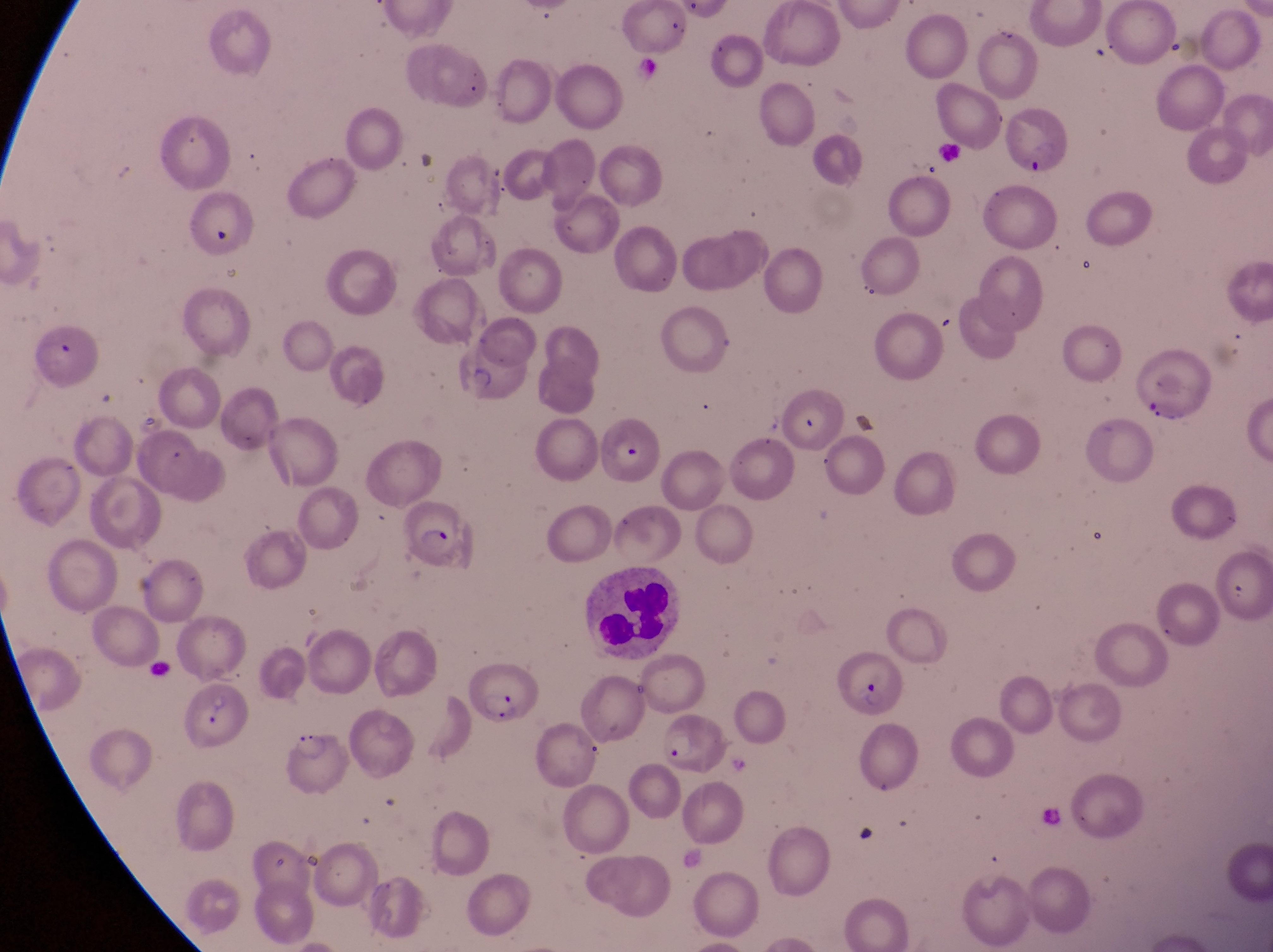

artifact (platelet-like body, stain precipitate, or debris) locations = approximate bounding boxes as [left, top, right, bottom] in pixels: [209, 222, 242, 254]
field of view = single
preparation = thin blood film
capture = smartphone photograph through the eyepiece of an Olympus CX-23 microscope
parasitised red blood cell locations = approximate bounding boxes as [left, top, right, bottom] in pixels: [1000, 109, 1074, 180], [30, 325, 95, 385], [447, 335, 534, 403], [594, 414, 657, 486], [395, 502, 473, 572], [838, 647, 908, 717], [459, 657, 546, 722], [183, 686, 245, 763], [657, 711, 732, 779], [284, 726, 346, 798]
leukocyte locations = approximate bounding boxes as [left, top, right, bottom] in pixels: [577, 569, 684, 662]
gametocyte locations = approximate bounding boxes as [left, top, right, bottom] in pixels: [426, 686, 474, 758]
magnification = 1000x
image size = 1273×952 pixels
country = Uganda